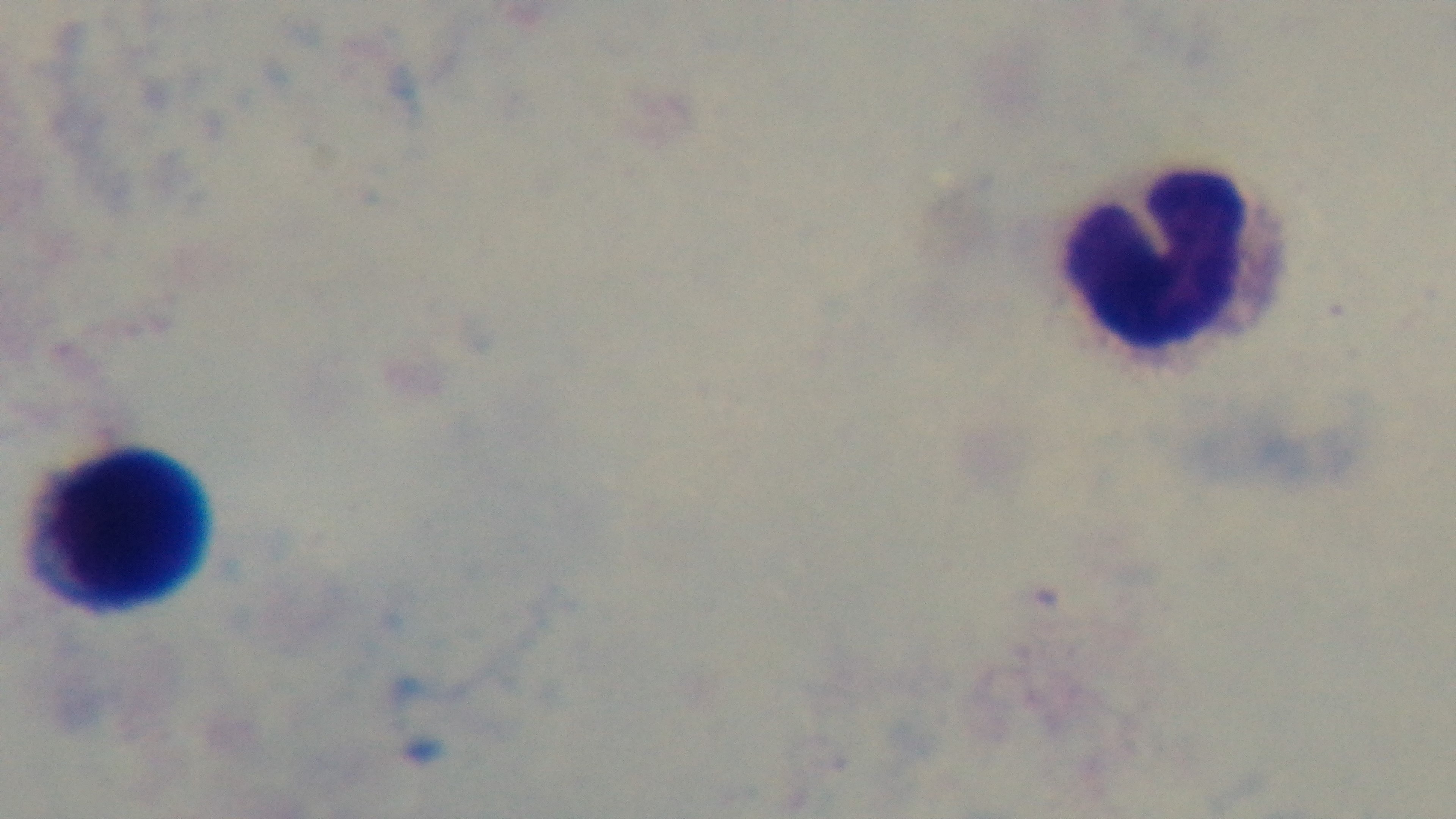
One field from the slide. Light microscopy. Oil-immersion objective, 100x. Mounted 4K digital camera. Giemsa stain. Malaria status: negative. Preparation: thick.